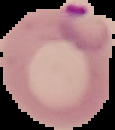

Summary:
  - Malaria status: parasitized
  - Image size: 115×130 pixels
  - Image type: cell region segmented out of the field of view; surrounding area masked to black
  - Preparation: thin blood smear